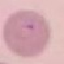

malaria status = parasitized
capture = smartphone camera at the microscope eyepiece
stain = Giemsa
image type = cell patch, automatically extracted from a larger field of view and resized to 64 × 64 pixels
preparation = thin blood film